Comment on the morphology of the red blood cells.
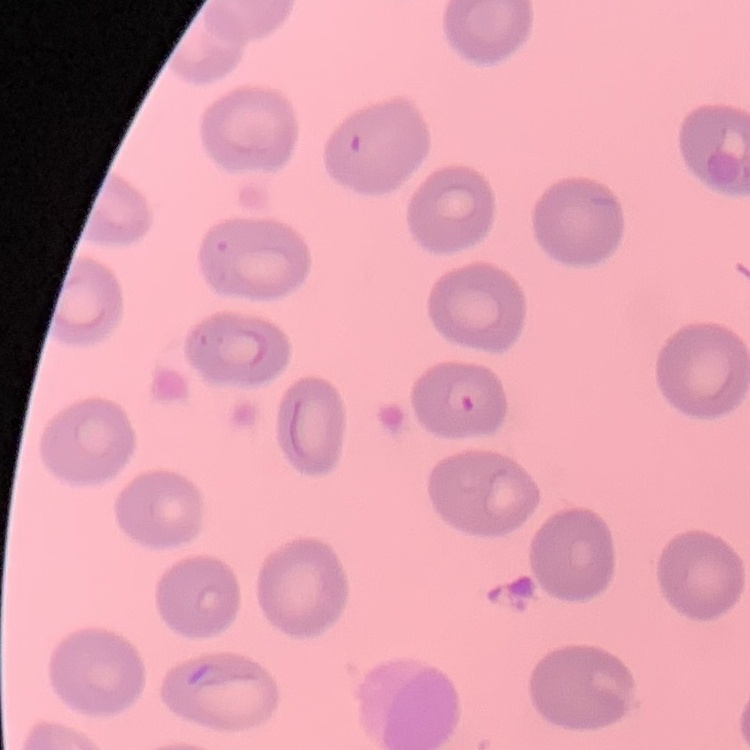
No rouleaux formation.

Square crop of a larger photomicrograph. Stained with either Field's or Giemsa. Thin peripheral smear.